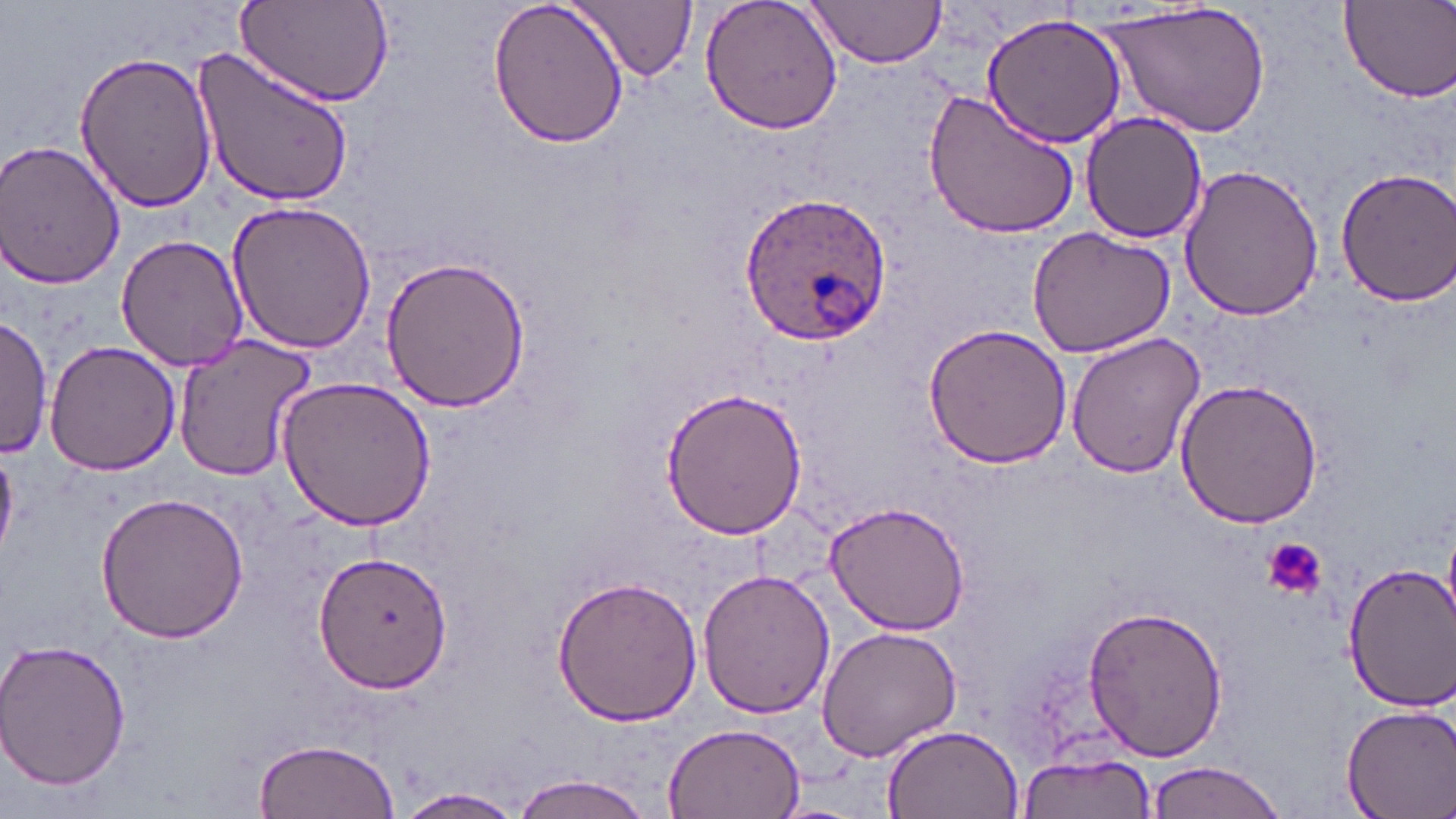

Summary:
  - Coordinate format: approximate bounding boxes as named x1/y1/x2/y2 corners in pixels
  - Platelet locations: (x1=1259, y1=538, x2=1326, y2=600)
  - Uninfected red blood cell locations: (x1=235, y1=0, x2=395, y2=110), (x1=487, y1=0, x2=630, y2=150), (x1=571, y1=0, x2=697, y2=82), (x1=699, y1=0, x2=846, y2=138), (x1=804, y1=1, x2=948, y2=68), (x1=1340, y1=1, x2=1455, y2=103), (x1=1105, y1=2, x2=1266, y2=139), (x1=982, y1=12, x2=1129, y2=148), (x1=190, y1=41, x2=355, y2=211), (x1=73, y1=48, x2=217, y2=214), (x1=922, y1=87, x2=1081, y2=241), (x1=1081, y1=111, x2=1208, y2=244), (x1=0, y1=139, x2=127, y2=290), (x1=1177, y1=163, x2=1324, y2=320), (x1=1331, y1=165, x2=1455, y2=309), (x1=226, y1=199, x2=376, y2=353), (x1=1027, y1=224, x2=1176, y2=358), (x1=115, y1=234, x2=249, y2=372), (x1=378, y1=254, x2=531, y2=414), (x1=0, y1=316, x2=52, y2=458), (x1=921, y1=322, x2=1072, y2=470), (x1=1066, y1=329, x2=1207, y2=479), (x1=171, y1=334, x2=318, y2=482), (x1=44, y1=340, x2=182, y2=475), (x1=276, y1=376, x2=439, y2=532), (x1=1175, y1=377, x2=1324, y2=529), (x1=658, y1=390, x2=807, y2=540), (x1=94, y1=491, x2=251, y2=643), (x1=825, y1=501, x2=970, y2=633), (x1=312, y1=548, x2=455, y2=693), (x1=1342, y1=561, x2=1454, y2=709), (x1=699, y1=567, x2=835, y2=719), (x1=551, y1=575, x2=703, y2=728), (x1=1084, y1=604, x2=1228, y2=763), (x1=817, y1=624, x2=961, y2=763), (x1=0, y1=637, x2=133, y2=790), (x1=1339, y1=703, x2=1456, y2=819), (x1=662, y1=721, x2=806, y2=817), (x1=881, y1=723, x2=1024, y2=817), (x1=250, y1=739, x2=402, y2=819), (x1=1014, y1=752, x2=1157, y2=819), (x1=1144, y1=762, x2=1289, y2=819), (x1=508, y1=773, x2=660, y2=818), (x1=396, y1=788, x2=533, y2=817)
  - Plasmodium ovale-infected red blood cell locations: (x1=734, y1=191, x2=893, y2=348)
  - Slide-level diagnosis: Plasmodium ovale
  - Image size: 1456×819 pixels
  - Field of view: single
  - Magnification: 1000x
  - Stain: May-Grünwald-Giemsa
  - Preparation: thin blood smear
  - Modality: optical microscopy